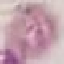
Result: no malaria parasites detected. Giemsa stain. Thin blood film. Automatically extracted cell patch, resized to 64 × 64 pixels. Acquired by smartphone through the microscope eyepiece.